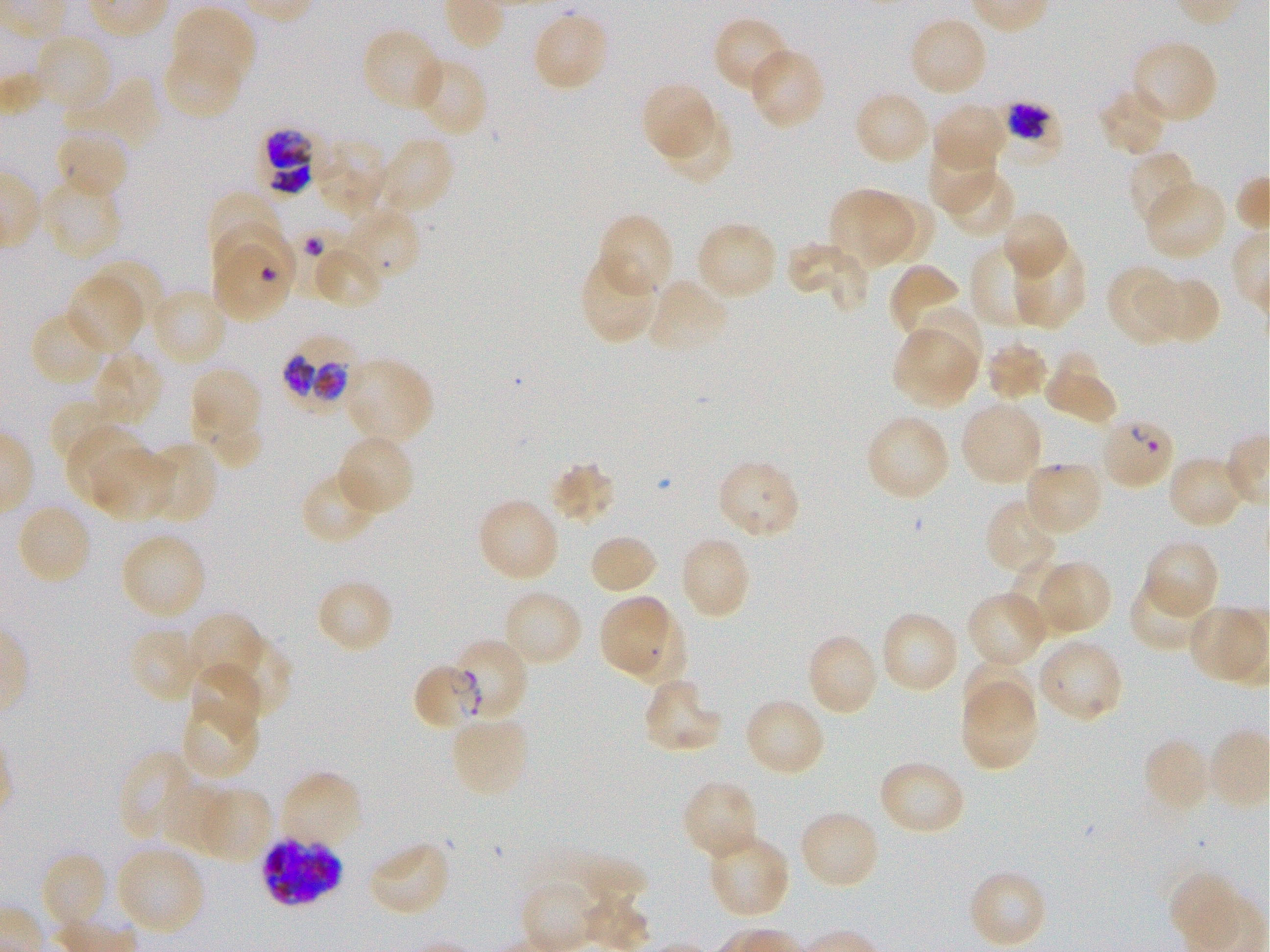
Approximate bounding boxes as (x1, y1, x2, y2) in pixels. Not every red blood cell is marked. Locations of infected red blood cells: (257, 128, 315, 196), (212, 246, 290, 322), (280, 333, 359, 407), (451, 637, 530, 723), (411, 663, 483, 732), (261, 835, 344, 907). Locations of red blood cells of indeterminate infection status: (995, 101, 1063, 167), (212, 224, 297, 300), (1098, 416, 1177, 490). Locations of uninfected red blood cells: (171, 7, 256, 89), (531, 10, 611, 93), (712, 17, 792, 94), (908, 17, 989, 98), (360, 27, 446, 113), (33, 33, 113, 114), (1131, 39, 1220, 125), (163, 46, 244, 120), (748, 47, 826, 130), (411, 57, 488, 138), (70, 76, 162, 149), (640, 82, 716, 162), (1097, 88, 1168, 157), (853, 91, 931, 167), (931, 103, 1008, 173), (662, 109, 733, 185), (53, 127, 130, 201), (377, 136, 455, 216), (313, 139, 389, 215), (928, 146, 995, 216), (1126, 149, 1197, 231), (942, 167, 1017, 239), (39, 177, 124, 261), (1144, 180, 1227, 261), (828, 189, 911, 268), (207, 191, 286, 269), (875, 196, 938, 263), (342, 207, 423, 283), (1001, 210, 1070, 281), (596, 212, 674, 297), (695, 221, 778, 301), (786, 240, 867, 309), (970, 241, 1048, 329), (1011, 241, 1086, 329), (313, 243, 384, 310), (577, 255, 659, 347), (89, 257, 167, 328), (887, 263, 963, 339), (1105, 264, 1180, 346), (1144, 274, 1221, 345), (66, 275, 143, 355), (646, 278, 730, 355), (147, 288, 229, 367), (912, 305, 983, 386), (31, 309, 110, 386), (891, 329, 974, 408), (984, 338, 1050, 403), (92, 351, 165, 428), (1044, 355, 1116, 422), (344, 357, 435, 445), (190, 367, 262, 444), (50, 396, 118, 465), (959, 401, 1044, 486), (199, 408, 263, 471), (865, 413, 951, 501), (65, 426, 147, 506), (337, 433, 415, 516), (144, 441, 219, 524), (93, 449, 173, 522), (1166, 453, 1245, 530), (715, 459, 803, 542), (548, 460, 617, 526), (1023, 460, 1104, 536), (300, 468, 383, 546), (476, 497, 561, 583), (984, 500, 1059, 576), (15, 502, 93, 586), (119, 533, 207, 620), (587, 533, 658, 596), (679, 535, 753, 620), (1142, 539, 1220, 619), (1010, 558, 1074, 628), (1033, 560, 1112, 636), (1128, 577, 1213, 652), (315, 578, 394, 654), (501, 588, 584, 668), (965, 591, 1050, 669), (599, 595, 666, 673), (1187, 605, 1267, 685), (618, 608, 687, 688), (879, 610, 961, 695), (185, 613, 265, 693), (127, 626, 200, 703), (805, 632, 880, 717), (221, 634, 292, 719), (1037, 637, 1124, 724), (961, 659, 1035, 728), (189, 660, 261, 737), (643, 679, 724, 755), (960, 684, 1038, 772), (181, 697, 261, 781), (743, 697, 826, 777), (449, 715, 531, 797), (1142, 736, 1213, 815), (118, 749, 197, 843), (877, 759, 966, 836), (280, 771, 364, 849), (681, 780, 760, 862), (159, 781, 232, 855), (197, 788, 273, 863), (798, 809, 880, 891), (707, 833, 791, 920), (367, 840, 453, 918), (116, 845, 206, 936), (40, 851, 110, 933), (579, 857, 647, 909), (967, 869, 1048, 949), (1167, 871, 1240, 943). Donor blood group O+. Thin blood smear. Giemsa stain. Image is 1270×952 pixels. Plasmodium falciparum strain 3D7 in static in-vitro culture. Single field of view. Oil immersion, 100x objective (numerical aperture 1.25).